Outline each blood parasite and name the species.
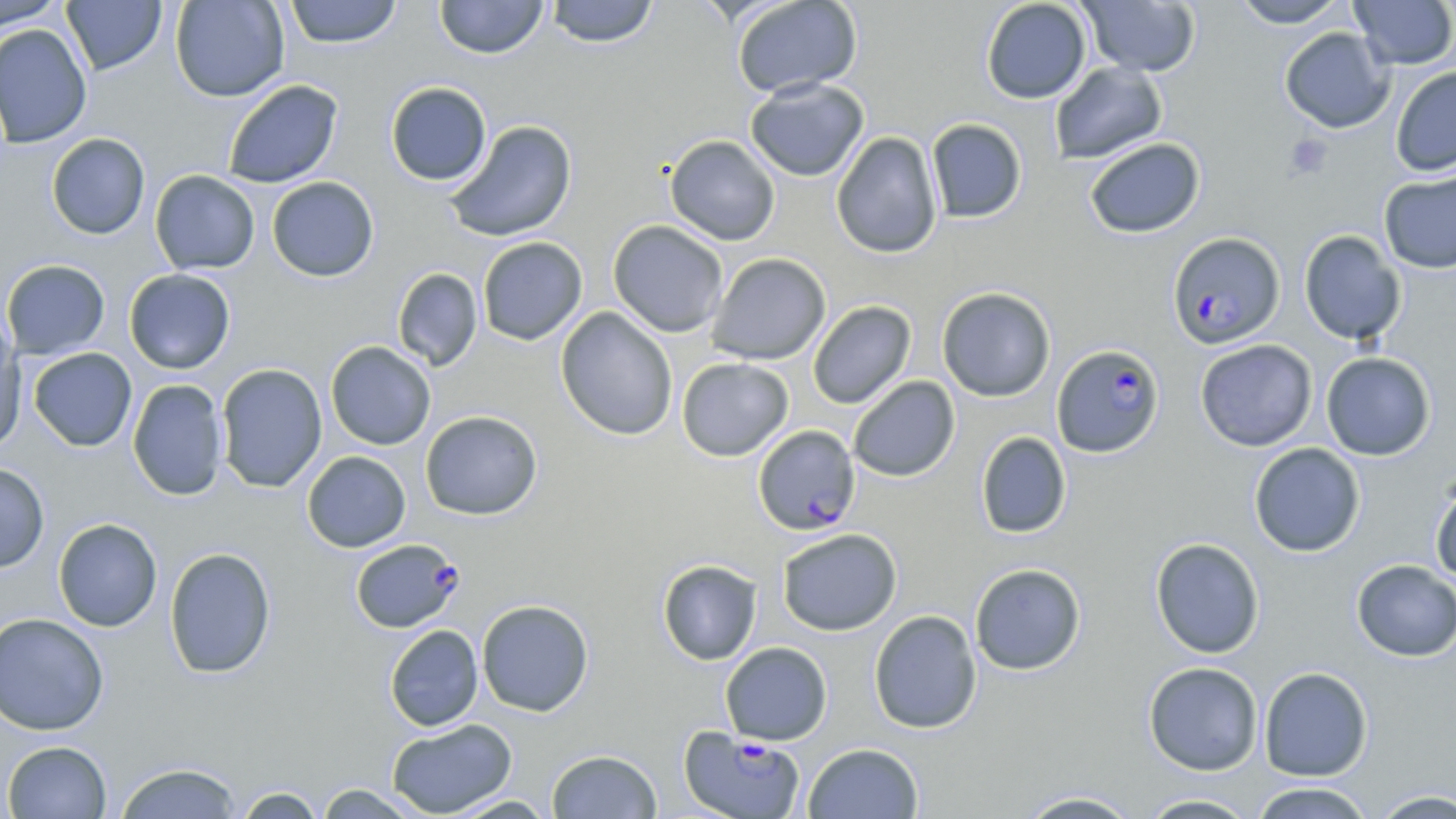
Approximate bounding boxes as (x1, y1, x2, y2) in pixels.
Plasmodium falciparum-infected red blood cells: (1167, 232, 1285, 350), (1051, 344, 1165, 458), (753, 424, 860, 536), (350, 538, 463, 633), (679, 727, 806, 819).
No Plasmodium ovale, Plasmodium malariae, Plasmodium vivax, Babesia divergens, or Trypanosoma brucei observed.

Platelet locations: (1284, 134, 1332, 180). Uninfected red blood cell locations: (0, 0, 67, 29), (61, 0, 167, 75), (170, 0, 289, 101), (434, 0, 548, 59), (731, 0, 863, 98), (980, 0, 1091, 104), (1232, 0, 1349, 28), (1349, 0, 1456, 70), (284, 1, 402, 48), (544, 1, 659, 48), (1078, 1, 1201, 77), (0, 23, 92, 149), (1279, 27, 1396, 134), (1049, 61, 1167, 165), (1390, 66, 1456, 177), (744, 77, 870, 182), (222, 79, 343, 188), (385, 81, 492, 186), (926, 118, 1028, 223), (444, 120, 578, 243), (830, 132, 943, 258), (46, 133, 150, 240), (664, 135, 781, 245), (1084, 138, 1205, 238), (1378, 168, 1456, 274), (149, 170, 261, 275), (266, 176, 379, 282), (607, 219, 729, 338), (1298, 230, 1406, 345), (477, 237, 588, 345), (706, 252, 831, 365), (1, 259, 110, 360), (391, 268, 483, 371), (124, 269, 236, 374), (936, 286, 1056, 402), (807, 300, 916, 409), (556, 307, 678, 441), (0, 326, 26, 454), (1195, 339, 1317, 451), (325, 341, 437, 451), (28, 348, 137, 451), (1320, 351, 1436, 461), (676, 357, 793, 462), (214, 363, 328, 493), (848, 376, 960, 482), (127, 378, 228, 501), (420, 410, 543, 520), (975, 431, 1072, 539), (1248, 442, 1365, 557), (302, 451, 411, 552), (0, 462, 50, 573), (1430, 475, 1456, 585), (53, 517, 163, 632), (777, 528, 902, 636), (1149, 537, 1265, 658), (164, 546, 276, 679), (657, 559, 763, 666), (1351, 559, 1456, 662), (969, 563, 1086, 676), (477, 599, 594, 717), (868, 609, 982, 734), (0, 612, 110, 735), (384, 625, 484, 731), (720, 641, 833, 745), (1143, 661, 1263, 775), (1258, 666, 1373, 781), (386, 718, 517, 818), (2, 740, 112, 818), (803, 742, 923, 818), (546, 749, 662, 819), (113, 761, 244, 818), (1248, 781, 1376, 819), (313, 783, 426, 818), (230, 786, 327, 818), (1367, 788, 1456, 818), (1013, 789, 1144, 818), (1137, 793, 1261, 818), (445, 794, 557, 818). Slide-level diagnosis: Plasmodium falciparum. Image is 1456×819 pixels. Single field of view. Light microscopy. May-Grünwald-Giemsa-stained preparation. 1000x magnification. Thin blood film.